Assess this cell for malaria.
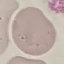

It is uninfected.

Summary:
  - Capture: smartphone through the microscope eyepiece
  - Preparation: thin smear
  - Stain: Giemsa
  - Image type: cell patch, automatically extracted from a larger field of view and resized to 64 × 64 pixels